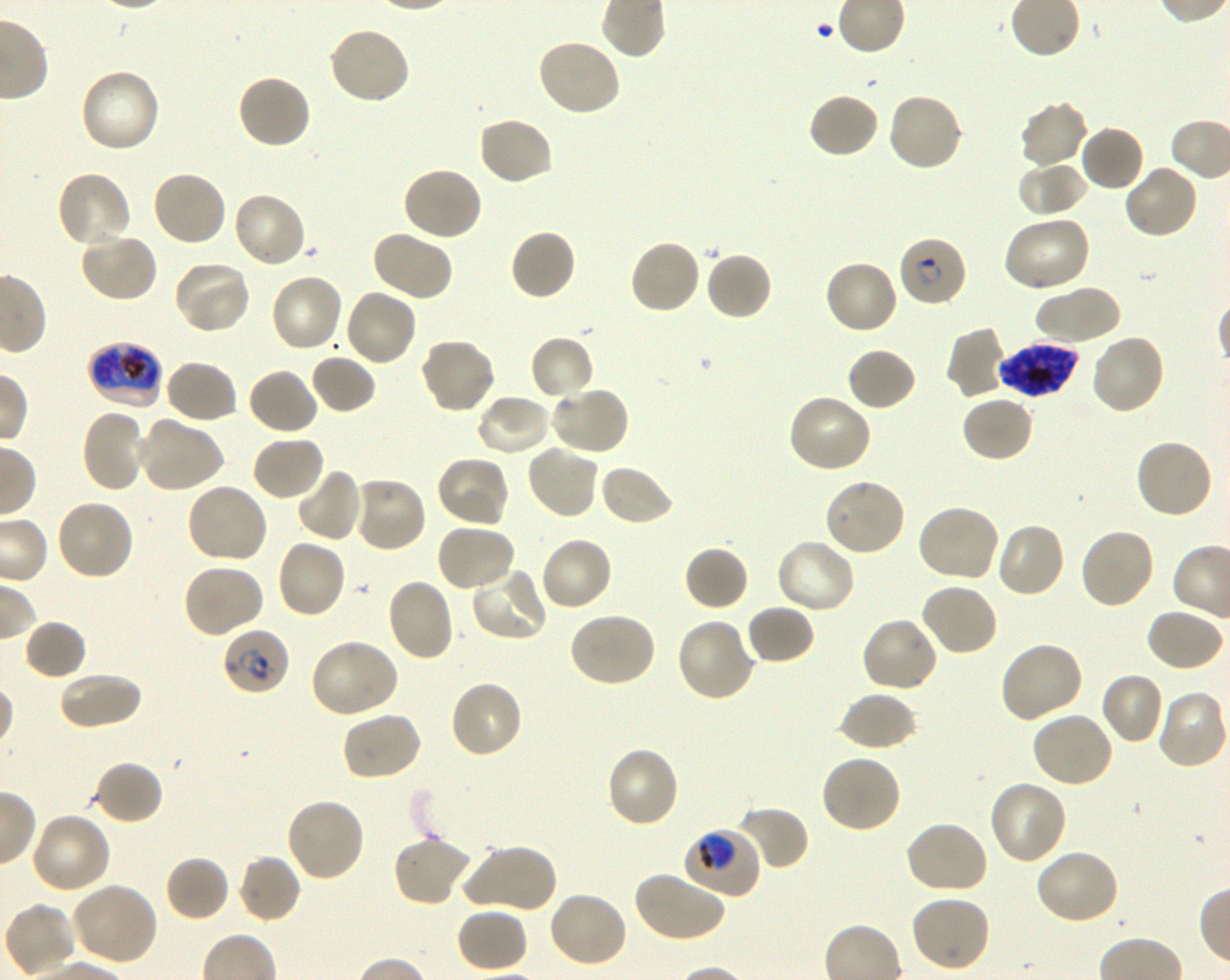
Approximate bounding boxes as [x1, y1, x2, y2] in pixels. Not every red blood cell is marked. A life-cycle stage — or a range of stages, where the recorded stages span more than one — follows each staged infected red blood cell.
Summary:
  - Locations of uninfected red blood cells: [326, 25, 412, 106], [536, 38, 623, 118], [78, 68, 162, 155], [235, 73, 312, 150], [808, 92, 880, 159], [886, 92, 964, 173], [1017, 100, 1089, 171], [476, 116, 555, 187], [1079, 125, 1146, 192], [1016, 160, 1088, 217], [1123, 163, 1200, 239], [402, 165, 484, 241], [54, 170, 133, 250], [151, 170, 227, 247], [232, 191, 308, 269], [1001, 214, 1092, 293], [509, 228, 577, 301], [79, 230, 159, 304], [370, 230, 454, 302], [628, 239, 701, 316], [704, 251, 773, 321], [822, 259, 898, 336], [172, 260, 252, 335], [269, 272, 345, 353], [1033, 284, 1120, 345], [343, 288, 418, 368], [946, 325, 1007, 398], [529, 334, 595, 401], [1089, 334, 1166, 416], [419, 336, 496, 415], [845, 346, 918, 412], [309, 354, 377, 414], [163, 359, 239, 424], [247, 367, 319, 437], [548, 385, 630, 456], [474, 393, 552, 457], [786, 393, 873, 473], [960, 395, 1035, 463], [80, 409, 149, 494], [136, 416, 224, 493], [251, 435, 326, 502], [1133, 437, 1213, 520], [526, 444, 600, 520], [435, 455, 512, 528], [598, 463, 675, 528], [296, 467, 364, 542], [349, 475, 427, 553], [824, 477, 907, 557], [185, 482, 269, 566], [54, 498, 134, 582], [915, 503, 1001, 583], [995, 522, 1067, 599], [435, 523, 518, 593], [1078, 527, 1156, 611], [539, 535, 613, 612], [775, 537, 856, 615], [275, 539, 347, 620], [683, 545, 749, 612], [182, 564, 265, 639], [469, 565, 549, 643], [385, 578, 456, 662], [919, 583, 999, 657], [745, 604, 815, 666], [1145, 607, 1226, 672], [567, 611, 657, 688], [860, 616, 939, 693], [675, 618, 757, 703], [23, 619, 88, 681], [309, 639, 400, 719], [998, 639, 1084, 724], [57, 670, 143, 732], [1099, 672, 1166, 745], [447, 679, 524, 760], [1155, 689, 1229, 770], [838, 690, 918, 752], [341, 710, 424, 782], [1030, 710, 1114, 789], [605, 746, 680, 829], [819, 754, 902, 834], [93, 760, 164, 825], [987, 780, 1068, 866], [284, 796, 366, 883], [736, 804, 809, 871], [30, 812, 112, 895], [904, 819, 988, 895], [392, 835, 473, 908], [463, 843, 558, 915], [1033, 847, 1120, 925], [236, 853, 303, 924], [164, 854, 231, 922], [632, 869, 727, 943], [69, 882, 159, 966], [546, 890, 629, 968], [910, 896, 991, 973], [3, 903, 79, 978], [455, 906, 529, 973]
  - Locations of infected red blood cells: [898, 235, 968, 307] early ring to early trophozoite; [86, 341, 164, 410] early trophozoite to late schizont; [998, 342, 1079, 398] schizont; [221, 628, 291, 697] early ring to early trophozoite; [682, 827, 762, 898] trophozoite
  - Life-cycle stages observed: trophozoite, schizont
  - Donor blood group: O+
  - Field of view: single
  - Culture: in-vitro Plasmodium falciparum strain 3D7, shaking
  - Preparation: thin blood smear
  - Image size: 1230×980 pixels
  - Objective: 100x, oil immersion, numerical aperture 1.30
  - Stain: Giemsa